Assess the morphology of the red blood cells.
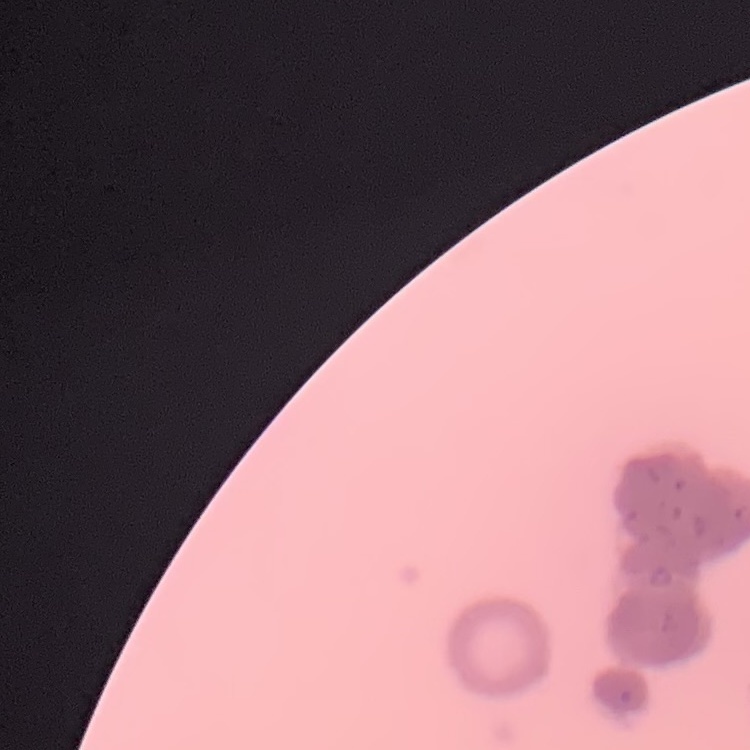
They show rouleaux formation.

Summary:
  - Preparation: thin peripheral smear
  - Image type: one tile cut from a larger photomicrograph
  - Stain: Field's or Giemsa